Classify this cell by malaria status.
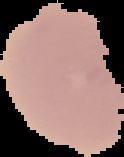

It is uninfected.

Summary:
  - Preparation: thin blood smear
  - Image size: 124×157 pixels
  - Image type: segmented cell region on a black background